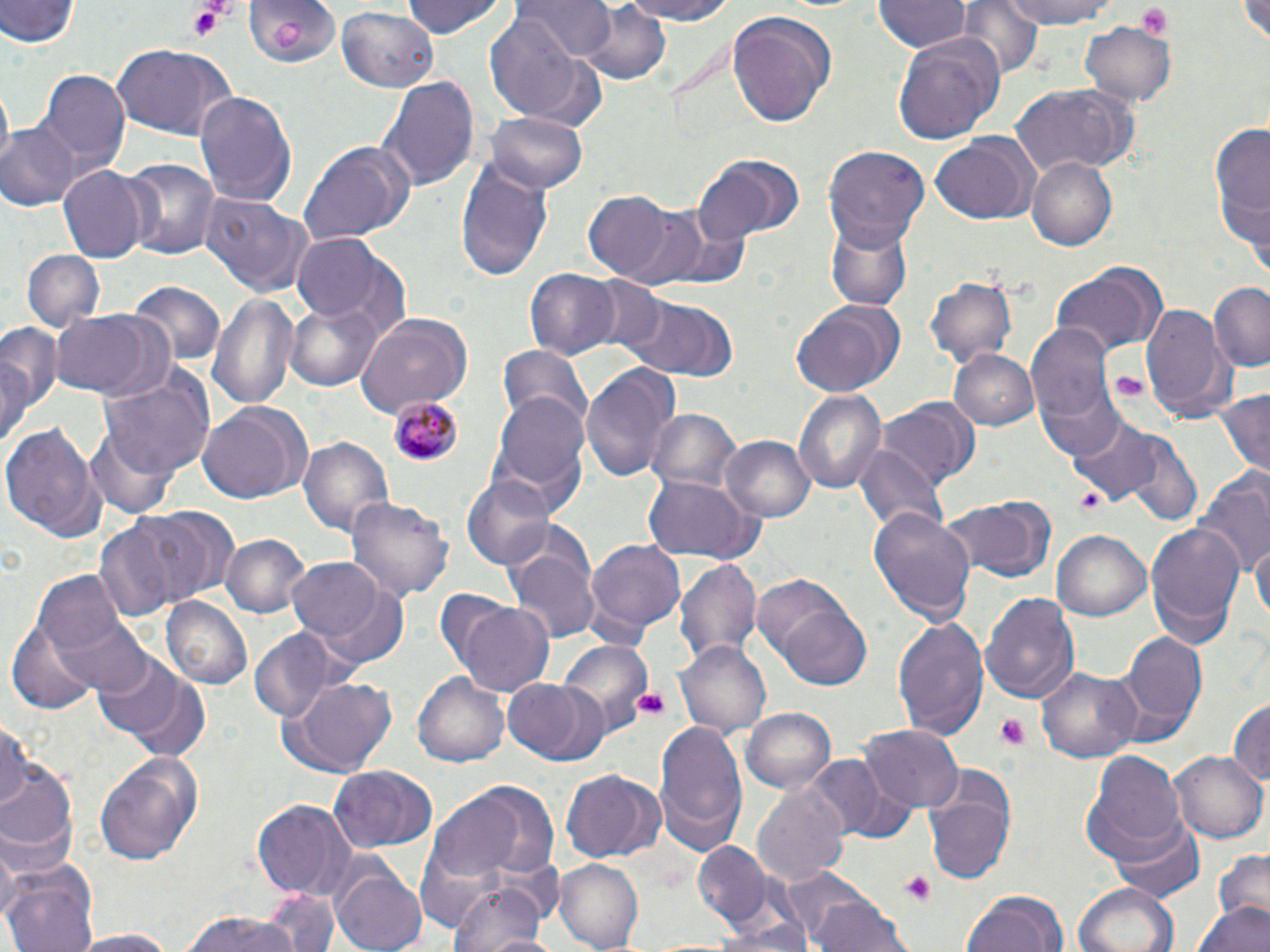

Approximate bounding boxes as (x1,y1)-(x2,y2) corner pairs in pixels. Platelet locations: (187,2)-(236,40), (1133,4)-(1174,39), (1109,368)-(1148,403), (1077,487)-(1106,517), (633,688)-(670,722), (994,714)-(1032,747), (901,873)-(936,903). Uninfected red blood cell locations: (0,0)-(78,50), (247,0)-(338,69), (398,0)-(511,41), (513,0)-(618,61), (609,0)-(744,24), (998,0)-(1119,29), (1234,0)-(1270,47), (874,1)-(967,53), (958,2)-(1043,80), (578,3)-(673,87), (336,8)-(435,91), (726,11)-(838,126), (482,17)-(594,120), (1080,21)-(1177,104), (891,33)-(1001,149), (108,43)-(239,141), (41,70)-(131,171), (380,73)-(478,191), (1011,83)-(1138,177), (1,87)-(14,163), (194,90)-(298,206), (483,111)-(589,193), (1208,120)-(1270,254), (0,122)-(80,212), (930,133)-(1038,225), (296,140)-(414,247), (825,146)-(931,248), (694,154)-(804,240), (1026,155)-(1118,251), (119,157)-(222,262), (455,158)-(553,281), (59,165)-(147,266), (201,192)-(316,299), (583,192)-(674,281), (606,201)-(718,291), (825,220)-(913,312), (289,232)-(408,337), (22,249)-(104,329), (1051,263)-(1168,359), (524,267)-(619,360), (926,276)-(1017,366), (586,278)-(667,359), (131,280)-(224,367), (1209,283)-(1270,374), (208,290)-(300,410), (625,294)-(740,382), (285,300)-(383,392), (790,300)-(905,396), (1141,301)-(1230,422), (52,308)-(166,402), (355,313)-(472,415), (0,322)-(55,454), (1026,325)-(1118,428), (498,345)-(591,430), (947,349)-(1039,432), (94,364)-(216,483), (580,364)-(678,486), (1215,388)-(1270,481), (794,390)-(885,495), (491,392)-(591,502), (881,398)-(979,487), (197,403)-(311,505), (645,408)-(741,500), (1067,414)-(1169,504), (0,420)-(103,541), (1096,426)-(1202,524), (721,434)-(815,521), (298,435)-(394,543), (857,444)-(948,537), (1193,473)-(1269,580), (462,475)-(552,568), (640,475)-(760,565), (346,496)-(453,602), (941,496)-(1056,584), (139,506)-(241,602), (869,506)-(974,626), (91,510)-(215,622), (1145,522)-(1245,645), (1054,531)-(1150,620), (221,535)-(307,618), (585,537)-(687,637), (1252,538)-(1268,630), (506,544)-(601,645), (285,555)-(396,656), (677,559)-(761,667), (754,572)-(870,686), (981,590)-(1078,706), (45,592)-(158,700), (163,598)-(251,689), (453,601)-(556,698), (893,616)-(989,739), (8,622)-(100,713), (248,628)-(344,724), (1121,631)-(1208,734), (554,638)-(653,730), (676,640)-(770,734), (96,655)-(208,757), (1037,664)-(1141,761), (415,672)-(511,768), (280,678)-(398,777), (503,679)-(609,766), (1228,697)-(1270,789), (740,707)-(836,796), (654,719)-(749,853), (0,721)-(29,810), (861,725)-(961,813), (1082,749)-(1186,859), (1171,750)-(1269,844), (96,754)-(205,864), (813,754)-(913,841), (0,761)-(78,866), (328,764)-(438,850), (561,769)-(655,863), (926,777)-(1015,882), (468,783)-(560,880), (754,783)-(849,889), (429,794)-(525,881), (253,798)-(357,897), (1108,818)-(1206,904), (0,832)-(22,928), (694,843)-(769,926), (1211,849)-(1270,925), (554,861)-(643,949), (333,864)-(430,952), (4,865)-(101,952), (780,867)-(892,951), (449,880)-(550,952), (1073,882)-(1179,952), (263,887)-(341,952), (960,890)-(1071,952), (814,898)-(911,952), (1195,900)-(1269,952), (178,909)-(301,952), (64,929)-(184,950). Plasmodium malariae-infected red blood cell locations: (389,394)-(461,467). Slide-level diagnosis: Plasmodium malariae. Thin blood film. Optical microscopy. Single field of view. Captured at 1000x magnification. Image is 1270×952 pixels. May-Grünwald-Giemsa stain.